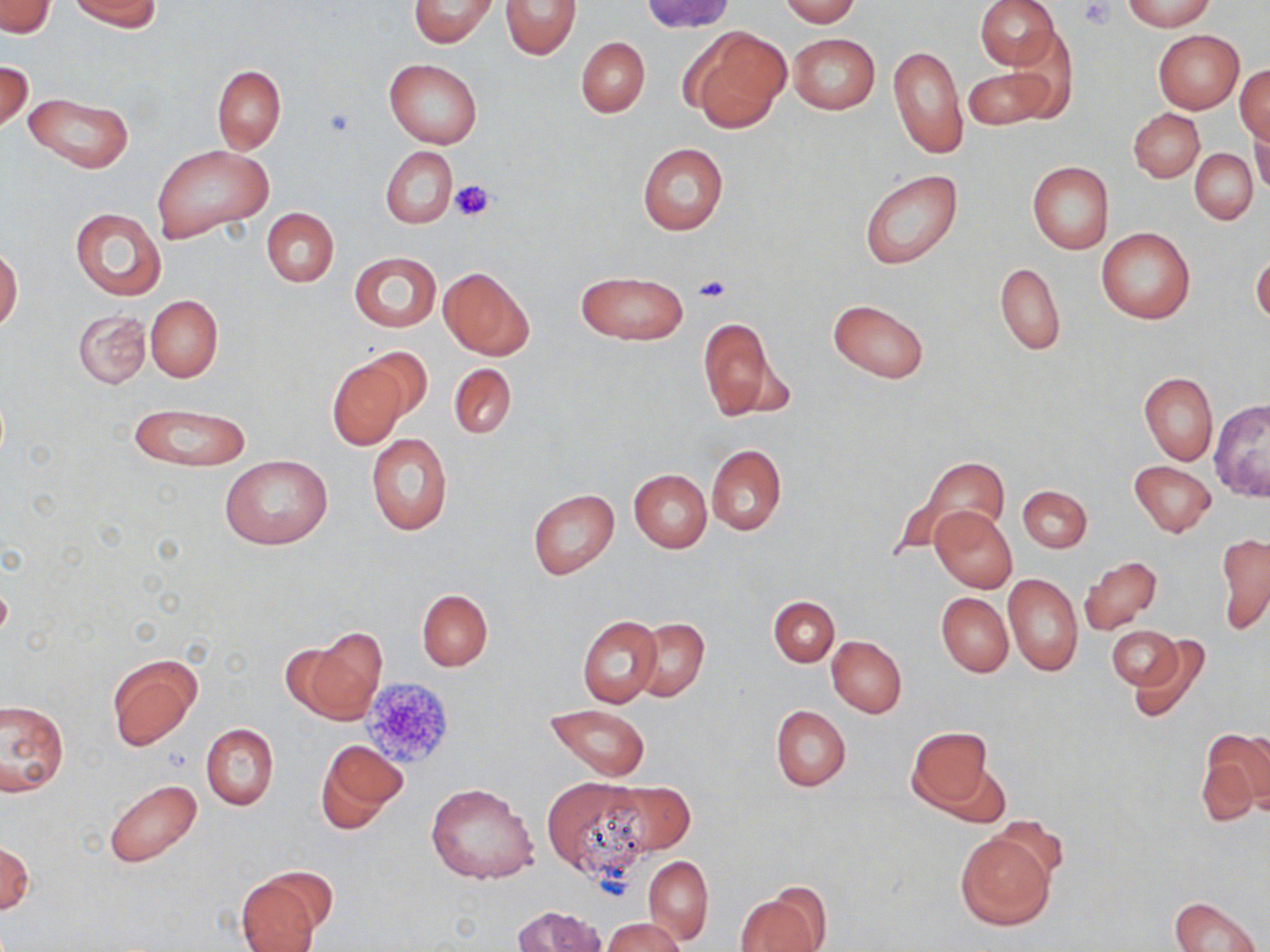

slide_level_diagnosis: negative for blood parasites
image_size: 1270×952 pixels
stain: May-Grünwald-Giemsa
field_of_view: one of a larger specimen
modality: optical microscopy
magnification: 1000x
platelet_locations: 'approximate bounding boxes as (x1, y1, x2, y2) in pixels: (1078, 1, 1117, 31), (449, 178, 497, 223), (694, 274, 732, 303), (361, 675, 456, 771)'
uninfected_red_blood_cell_locations: 'approximate bounding boxes as (x1, y1, x2, y2) in pixels: (70, 0, 161, 31), (408, 0, 499, 48), (780, 0, 861, 25), (976, 0, 1060, 70), (1122, 0, 1213, 31), (500, 1, 581, 60), (642, 1, 733, 35), (0, 2, 55, 37), (682, 24, 789, 131), (1153, 29, 1245, 113), (788, 32, 881, 114), (576, 37, 651, 118), (998, 37, 1076, 122), (889, 45, 968, 157), (384, 57, 482, 149), (0, 59, 33, 131), (213, 65, 286, 152), (1234, 65, 1270, 143), (964, 67, 1053, 129), (23, 92, 133, 172), (1129, 109, 1203, 182), (1248, 125, 1268, 194), (637, 143, 729, 235), (152, 144, 273, 243), (381, 145, 455, 228), (1190, 148, 1258, 224), (1027, 161, 1114, 255), (860, 170, 964, 271), (261, 207, 338, 287), (70, 208, 167, 301), (1097, 228, 1194, 323), (0, 248, 22, 330), (349, 252, 440, 331), (1252, 253, 1270, 324), (996, 262, 1065, 354), (439, 268, 533, 359), (574, 270, 687, 346), (146, 295, 222, 381), (828, 298, 929, 383), (73, 309, 149, 388), (697, 318, 786, 423), (361, 346, 434, 423), (325, 355, 413, 450), (449, 362, 516, 441), (1140, 371, 1217, 465), (1208, 400, 1270, 502), (128, 403, 251, 472), (366, 433, 453, 536), (706, 445, 787, 534), (896, 453, 1009, 552), (221, 455, 331, 550), (1129, 461, 1216, 537), (629, 469, 712, 552), (1018, 485, 1091, 552), (527, 489, 619, 581), (930, 506, 1017, 593), (1216, 532, 1270, 636), (1079, 558, 1162, 635), (1003, 573, 1083, 676), (417, 589, 492, 671), (937, 592, 1013, 677), (768, 596, 839, 667), (578, 616, 662, 708), (634, 618, 709, 702), (1108, 625, 1182, 689), (300, 627, 387, 723), (1128, 635, 1213, 723), (827, 636, 907, 717), (107, 655, 201, 749), (2, 699, 68, 796), (545, 704, 652, 782), (771, 705, 851, 791), (201, 723, 279, 810), (906, 726, 993, 812), (1199, 728, 1270, 822), (316, 739, 406, 833), (933, 759, 1012, 829), (543, 778, 651, 878), (603, 779, 694, 855), (105, 782, 201, 868), (425, 782, 540, 885), (955, 830, 1056, 929), (0, 841, 33, 918), (643, 856, 713, 943), (233, 872, 327, 952), (736, 889, 826, 951), (1170, 895, 1262, 952), (509, 905, 609, 952), (603, 918, 686, 952)'
preparation: thin blood film